Outline each Trypanosoma brucei.
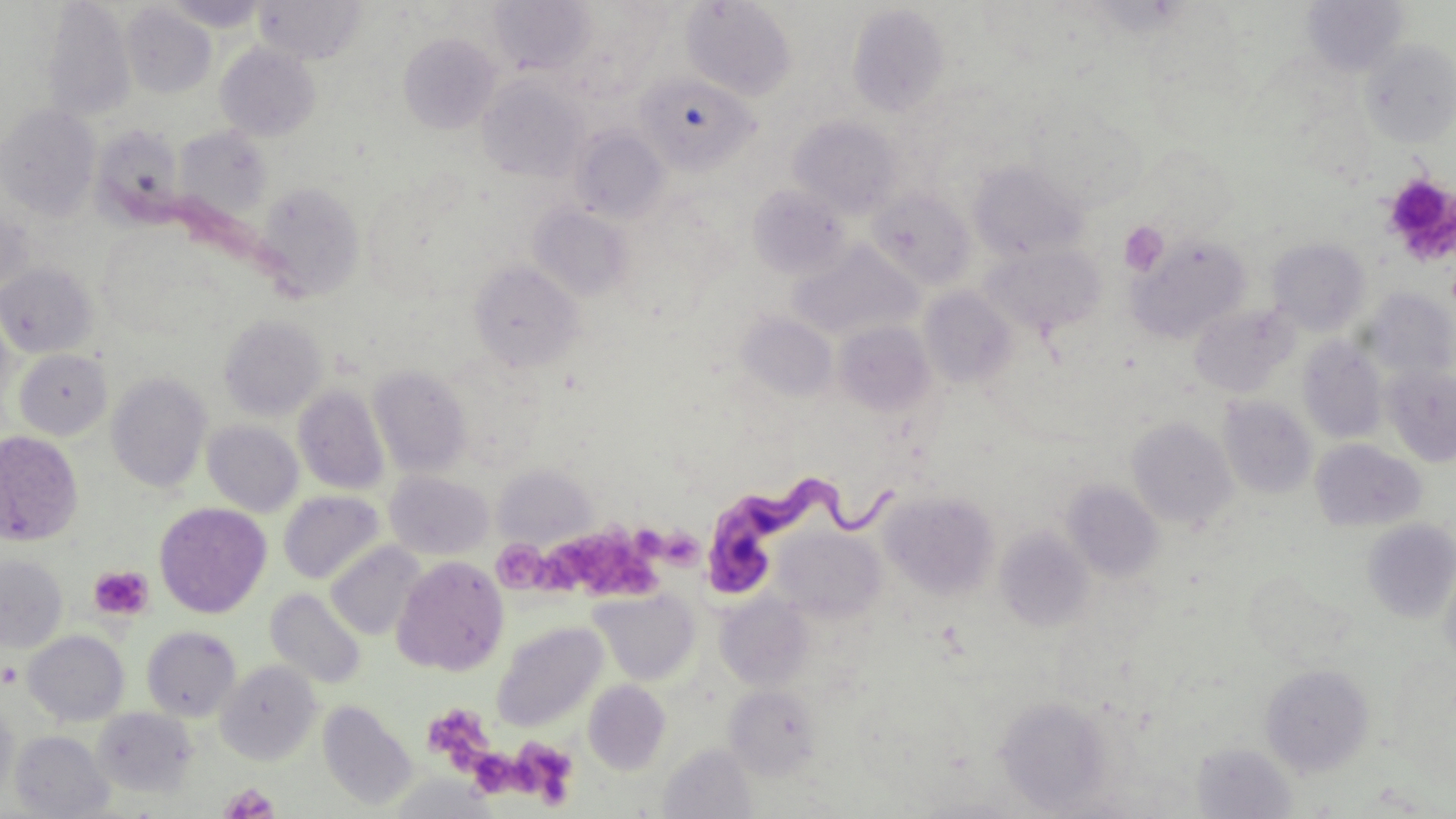

Approximate bounding boxes as [x1, y1, x2, y2] in pixels.
Trypanosoma brucei: [702, 476, 898, 599].

Uninfected red blood cell locations: [160, 0, 269, 32], [253, 0, 367, 64], [487, 0, 597, 75], [681, 0, 798, 100], [1300, 0, 1409, 77], [41, 1, 137, 122], [121, 3, 217, 98], [549, 3, 666, 100], [847, 4, 950, 118], [399, 32, 501, 134], [1360, 38, 1456, 147], [215, 43, 321, 141], [635, 73, 758, 174], [477, 75, 589, 183], [0, 104, 100, 221], [789, 116, 905, 218], [92, 124, 186, 227], [569, 126, 670, 224], [173, 127, 272, 223], [968, 159, 1087, 261], [256, 181, 365, 301], [747, 184, 850, 278], [866, 188, 975, 289], [530, 204, 633, 302], [0, 205, 34, 301], [1129, 235, 1250, 342], [1267, 237, 1371, 335], [788, 240, 921, 342], [983, 245, 1106, 337], [470, 261, 584, 372], [0, 262, 97, 358], [919, 287, 1017, 389], [1363, 289, 1455, 382], [1188, 302, 1297, 398], [737, 311, 838, 403], [219, 314, 327, 420], [834, 321, 935, 416], [1298, 336, 1388, 444], [14, 348, 113, 441], [1383, 363, 1456, 467], [368, 364, 472, 477], [106, 372, 212, 493], [293, 385, 389, 495], [1218, 396, 1317, 498], [1127, 416, 1238, 529], [202, 420, 303, 517], [0, 430, 83, 546], [1310, 439, 1426, 532], [493, 464, 596, 549], [385, 471, 494, 560], [1063, 481, 1164, 582], [279, 490, 386, 585], [880, 490, 999, 600], [154, 502, 271, 618], [296, 506, 416, 613], [1361, 519, 1456, 624], [995, 528, 1096, 631], [773, 529, 886, 623], [326, 542, 426, 641], [0, 555, 68, 652], [392, 555, 509, 676], [1439, 556, 1456, 678], [1243, 570, 1355, 668], [265, 588, 367, 690], [589, 588, 700, 686], [715, 591, 814, 690], [492, 621, 608, 732], [141, 625, 241, 721], [23, 630, 130, 726], [215, 660, 322, 766], [1259, 663, 1374, 776], [584, 680, 670, 775], [724, 685, 822, 780], [995, 696, 1114, 811], [0, 697, 19, 806], [318, 700, 418, 812], [92, 707, 198, 798], [9, 730, 114, 818], [1192, 741, 1297, 818], [659, 743, 756, 819], [389, 775, 499, 817], [907, 793, 1034, 817]. Platelet locations: [1383, 173, 1456, 263], [1120, 221, 1168, 276], [550, 533, 662, 595], [662, 534, 706, 582], [492, 538, 550, 593], [88, 565, 154, 621], [422, 703, 494, 771], [519, 741, 579, 809], [467, 749, 526, 798], [219, 783, 280, 819]. Slide-level diagnosis: Trypanosoma brucei. Image is 1456×819 pixels. Thin blood film. Captured at 1000x magnification. May-Grünwald-Giemsa-stained preparation. Single field of view. Light microscopy.